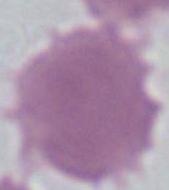

Summary:
  - Modality: photomicrograph
  - Magnification: 1000x
  - Identification: erythrocyte